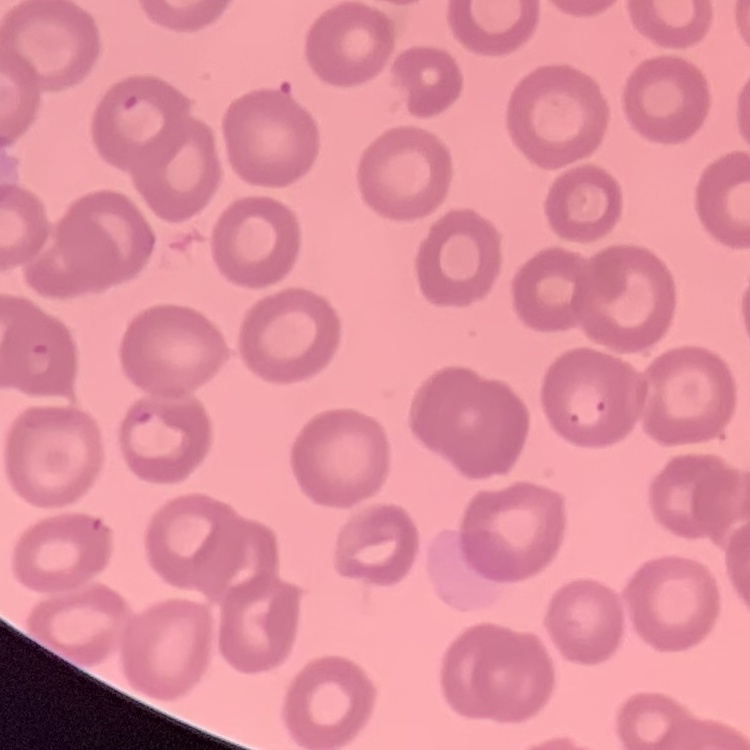
The erythrocytes exhibit no rouleaux formation. Square crop of a larger photomicrograph. Stained with either Field's or Giemsa. Thin peripheral smear.